Assess the morphology of the erythrocytes.
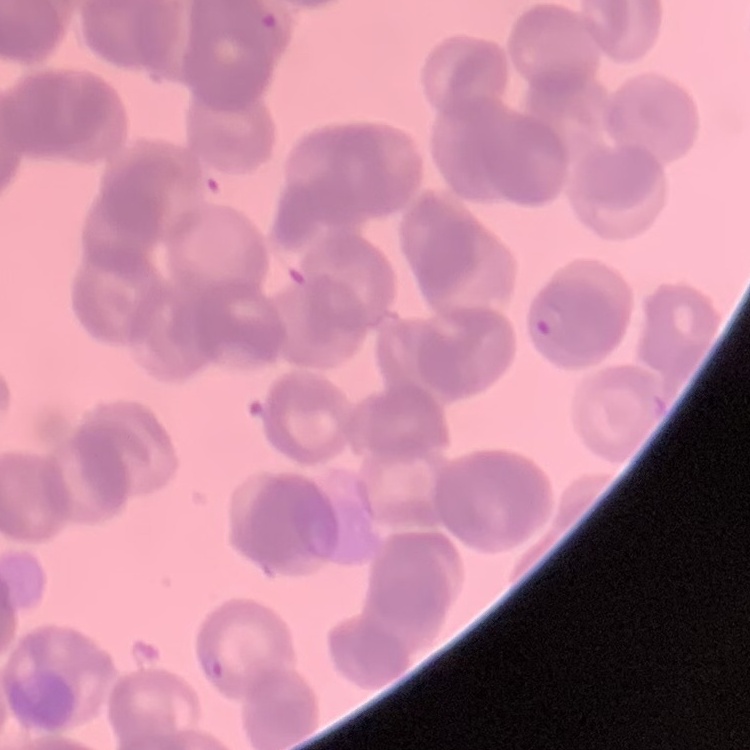

Rouleaux formation.

Thin blood smear. One tile cut from a larger photomicrograph. Field's or Giemsa stain.